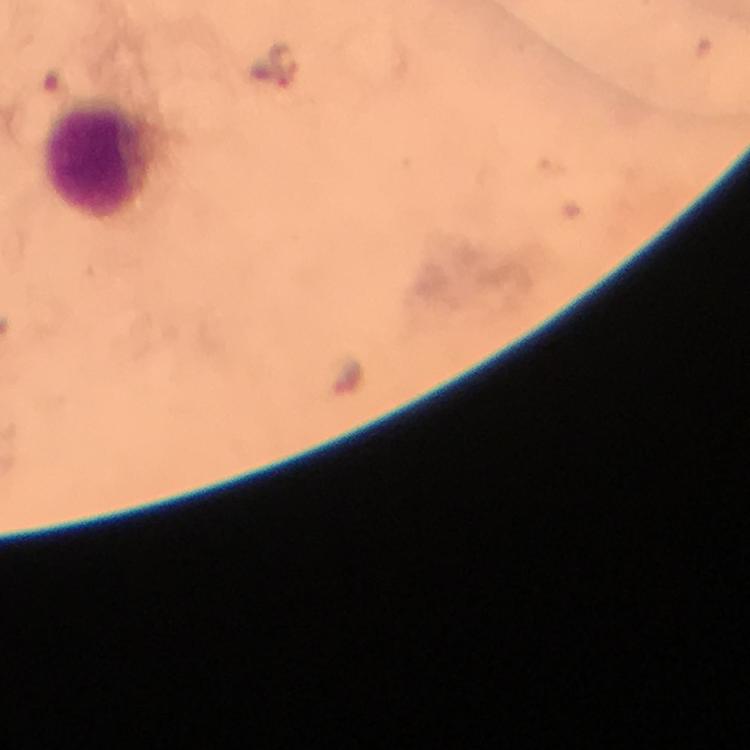

Approximate centers as (x, y) in pixels.
Summary:
  - Plasmodium parasite locations: (285, 68)
  - Leukocyte locations: (93, 156)
  - Stain: Giemsa
  - Magnification: 100x
  - Cropped from: a single field of view
  - Image size: 750×750 pixels
  - Immersion oil: applied
  - Context: from a malaria diagnostic workup
  - Capture: smartphone mounted on the microscope
  - Preparation: thick smear